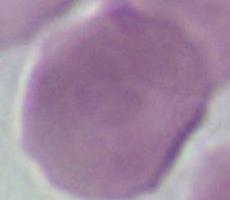
modality = micrograph
identification = red blood cell
magnification = 1000x